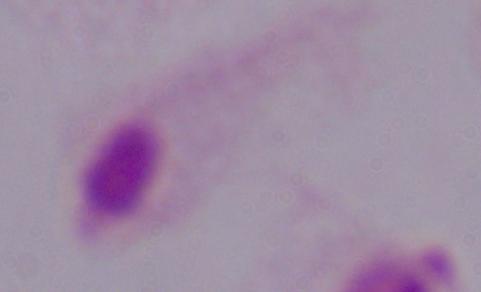
identification = trichomonad
modality = photomicrograph
magnification = 1000x